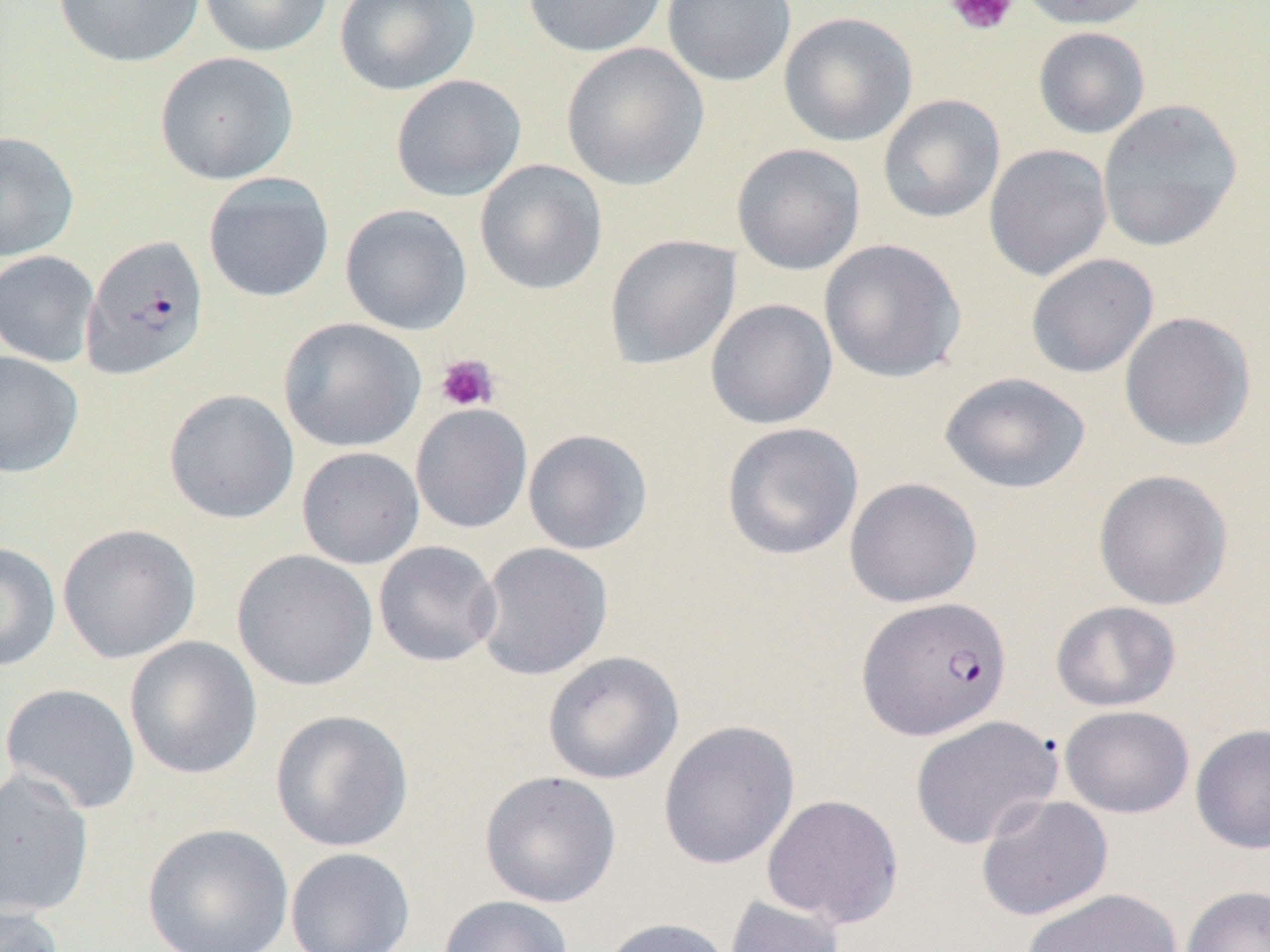
Summary:
  - Coordinate format: approximate bounding boxes as [x1, y1, x2, y2] in pixels
  - Platelet locations: [944, 0, 1020, 37], [436, 353, 500, 412]
  - Uninfected red blood cell locations: [51, 0, 206, 68], [197, 0, 334, 58], [334, 0, 480, 95], [521, 0, 670, 58], [662, 0, 796, 87], [1016, 0, 1154, 30], [778, 12, 918, 147], [1033, 26, 1150, 139], [561, 42, 709, 191], [154, 51, 299, 185], [390, 73, 527, 202], [878, 94, 1006, 224], [1097, 99, 1243, 253], [0, 131, 80, 261], [732, 143, 866, 275], [983, 144, 1113, 281], [474, 159, 608, 295], [202, 172, 335, 302], [340, 203, 472, 335], [604, 234, 741, 370], [819, 238, 967, 384], [0, 250, 100, 367], [1025, 253, 1159, 379], [705, 298, 838, 430], [1118, 311, 1257, 452], [279, 317, 426, 453], [0, 351, 84, 478], [939, 371, 1091, 494], [163, 389, 299, 524], [410, 403, 533, 534], [720, 422, 864, 560], [522, 428, 654, 555], [296, 446, 425, 570], [1092, 469, 1234, 611], [844, 476, 983, 608], [57, 523, 201, 664], [373, 540, 502, 667], [0, 541, 61, 672], [474, 542, 614, 681], [232, 549, 379, 692], [1050, 600, 1182, 712], [123, 635, 262, 780], [542, 650, 684, 785], [0, 682, 142, 815], [1059, 705, 1195, 819], [269, 709, 413, 852], [909, 715, 1063, 850], [657, 719, 800, 870], [1189, 723, 1270, 854], [0, 768, 95, 918], [479, 770, 622, 908], [762, 793, 904, 929], [975, 794, 1114, 922], [141, 822, 295, 952], [285, 847, 416, 952], [1180, 885, 1270, 952], [1021, 888, 1183, 952], [724, 894, 847, 952], [437, 895, 574, 952], [0, 903, 65, 952], [596, 917, 735, 952]
  - Plasmodium falciparum-infected red blood cell locations: [81, 234, 210, 381], [856, 595, 1012, 741]
  - Slide-level diagnosis: Plasmodium falciparum
  - Magnification: 1000x
  - Preparation: thin blood smear
  - Image size: 1270×952 pixels
  - Modality: light microscopy
  - Field of view: one of a larger specimen